Point out each malaria parasite.
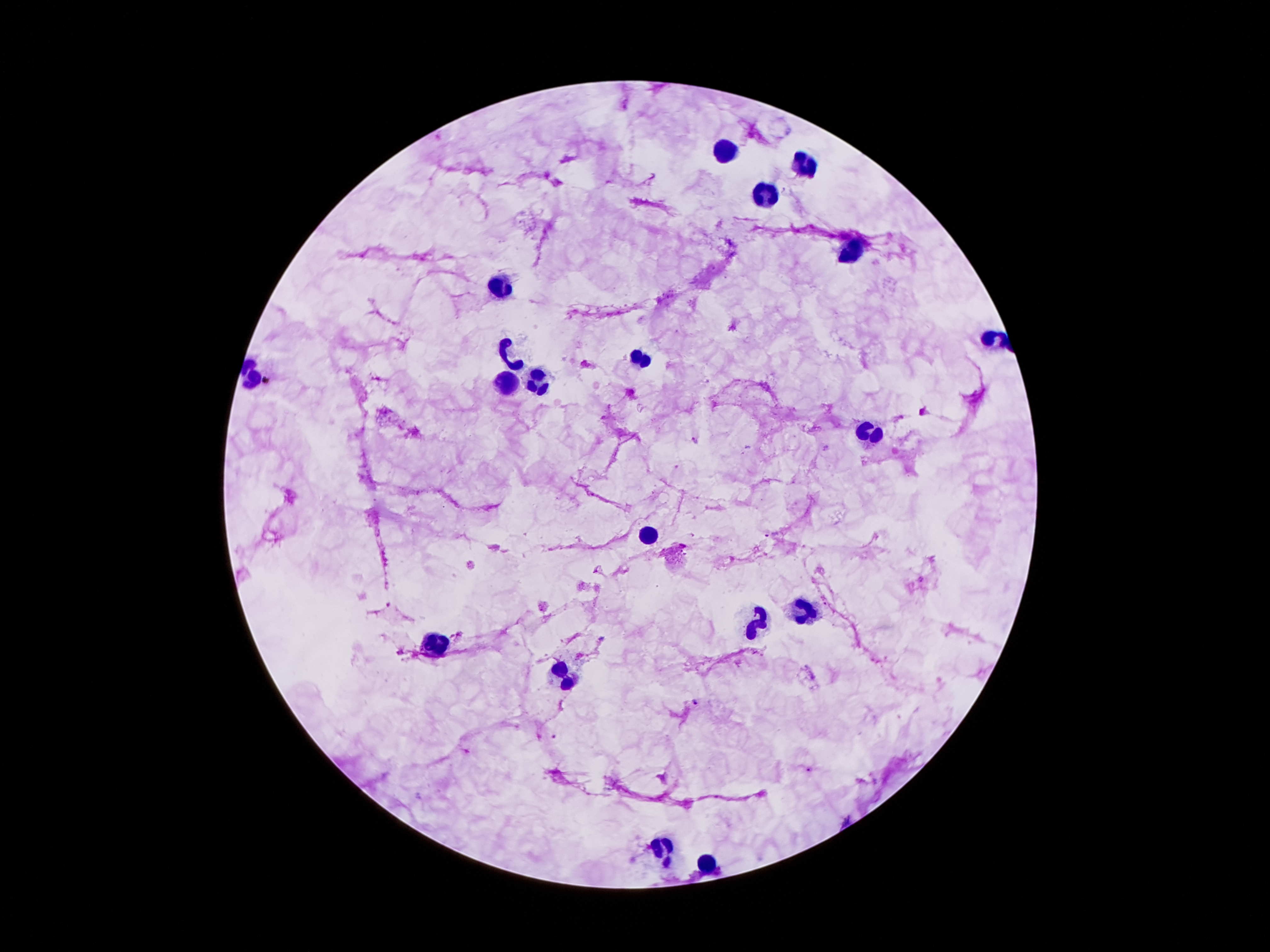

Approximate centers as (x, y) in pixels.
Malaria parasites: (697, 440), (460, 635), (695, 703), (555, 737), (810, 769).

Summary:
  - Leukocyte locations: (721, 151), (802, 164), (764, 195), (848, 254), (502, 284), (991, 336), (514, 358), (639, 360), (541, 379), (509, 383), (870, 433), (646, 535), (802, 608), (752, 625), (432, 642), (559, 676), (666, 850), (707, 864)
  - Capture: smartphone camera through the microscope eyepiece
  - Patient malaria status: infected with Plasmodium falciparum
  - Field of view: one from this slide
  - Preparation: thick blood smear
  - Stain: Giemsa
  - Image size: 1270×952 pixels
  - Magnification: 100x